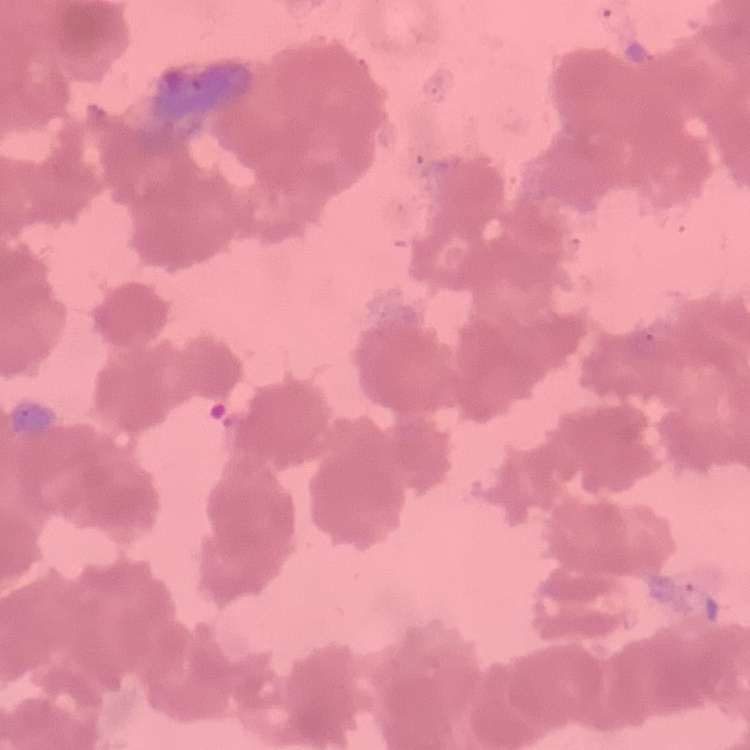

Summary:
  - Erythrocyte morphology: rouleaux formation
  - Stain: Field's or Giemsa
  - Preparation: thin blood film
  - Image type: square crop of a larger photomicrograph